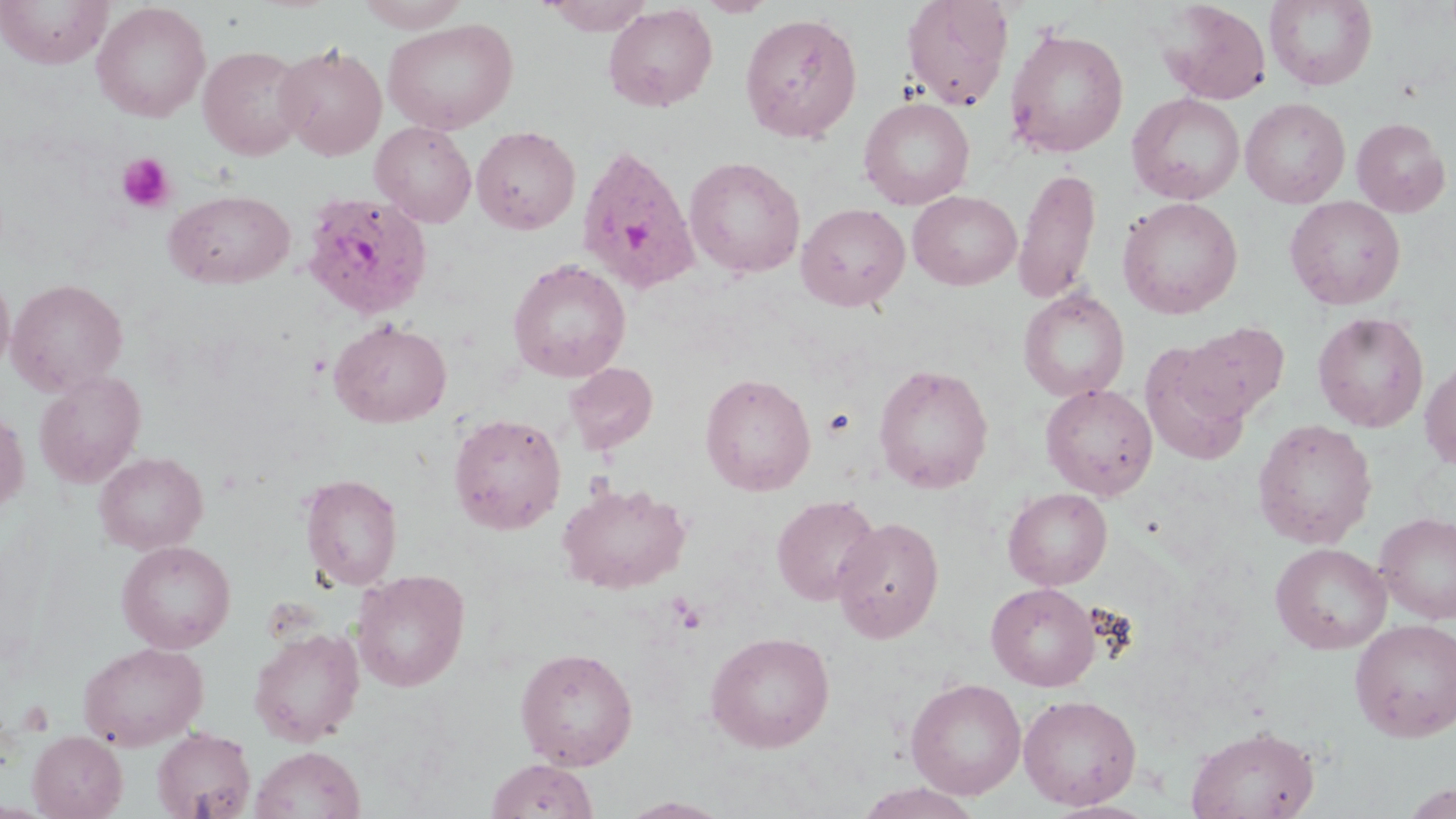
Approximate bounding boxes as (x1,y1)-(x2,y2) corner pairs in pixels. Uninfected red blood cell locations: (0,0)-(113,68), (353,0)-(472,31), (538,0)-(655,35), (696,0)-(777,17), (1264,0)-(1378,90), (900,1)-(1014,111), (1158,1)-(1272,105), (92,2)-(211,122), (603,3)-(717,112), (739,12)-(863,143), (383,18)-(519,134), (1004,25)-(1129,158), (275,43)-(387,160), (198,45)-(309,160), (1127,92)-(1245,205), (858,97)-(975,210), (1240,97)-(1350,208), (1351,117)-(1451,217), (370,121)-(477,227), (472,126)-(580,234), (684,156)-(806,278), (1014,166)-(1101,304), (165,189)-(295,288), (908,190)-(1021,290), (1284,195)-(1406,310), (1117,196)-(1243,319), (796,202)-(910,312), (507,258)-(631,383), (0,268)-(15,379), (6,278)-(128,395), (1018,288)-(1130,401), (1313,311)-(1429,432), (329,319)-(451,428), (1175,321)-(1291,428), (1139,337)-(1257,465), (1419,355)-(1456,470), (564,362)-(658,454), (873,363)-(994,494), (34,371)-(146,488), (700,372)-(816,496), (1040,383)-(1158,500), (0,407)-(29,517), (448,412)-(567,534), (1253,418)-(1378,549), (94,451)-(208,555), (299,474)-(403,591), (557,481)-(692,594), (1003,487)-(1112,590), (771,495)-(882,606), (1374,511)-(1456,625), (832,516)-(945,644), (117,540)-(236,653), (1270,542)-(1392,655), (352,569)-(471,692), (986,582)-(1100,691), (1350,619)-(1456,741), (248,627)-(364,746), (705,631)-(835,753), (78,641)-(209,751), (515,646)-(638,770), (906,677)-(1027,800), (1018,694)-(1142,810), (1186,724)-(1320,819), (151,726)-(257,819), (28,730)-(127,818), (250,746)-(365,819), (485,757)-(598,818), (854,782)-(984,819), (617,797)-(735,819). Platelet locations: (116,153)-(175,213), (822,408)-(856,438), (672,598)-(707,634). Plasmodium ovale-infected red blood cell locations: (575,143)-(701,295), (302,191)-(434,320). Slide-level diagnosis: Plasmodium ovale. Thin blood smear. Optical microscopy. One field of a larger specimen. 1000x magnification. May-Grünwald-Giemsa stain. Image is 1456×819 pixels.